Give the preparation type.
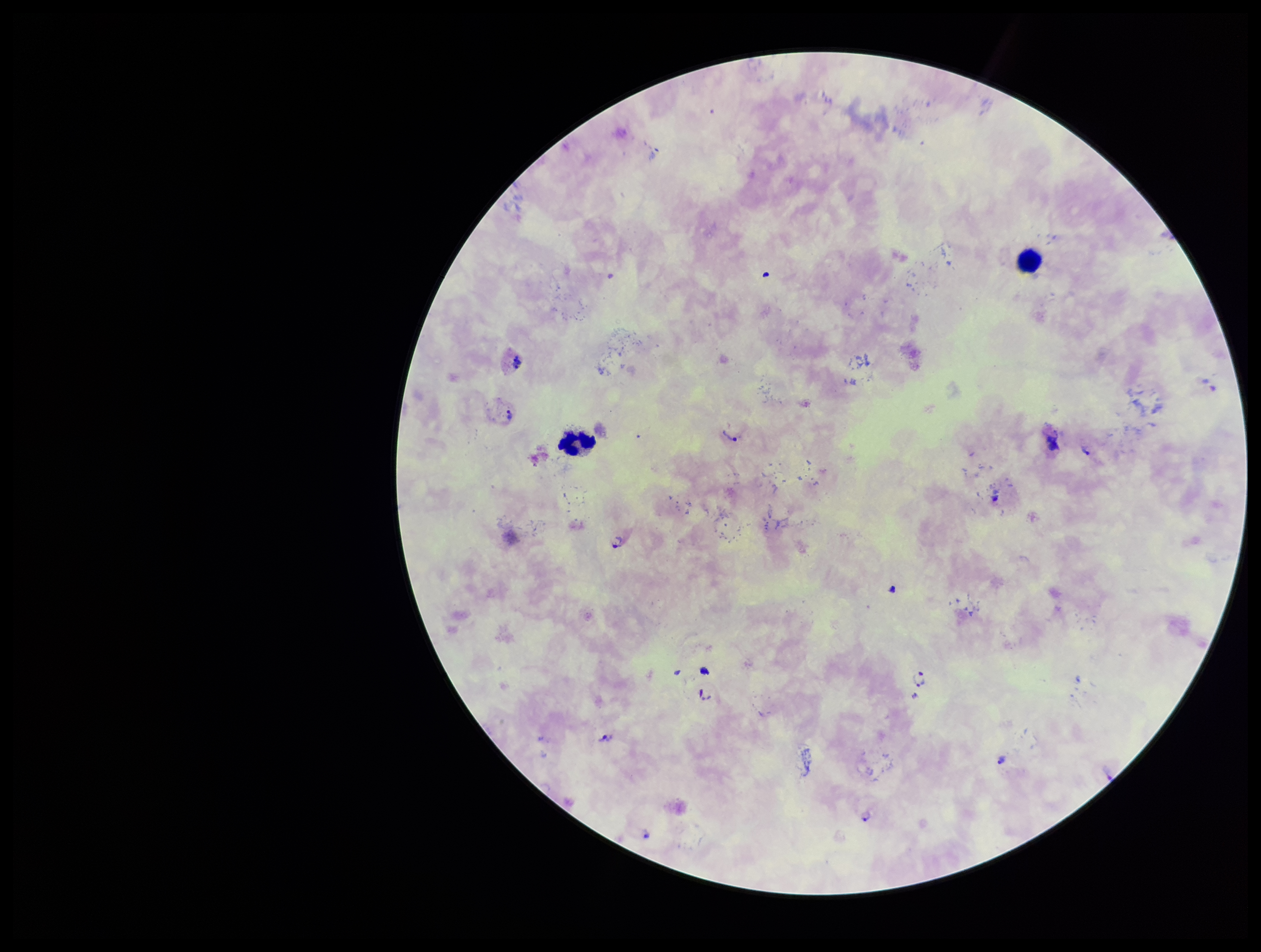

A thick smear.

Plasmodium parasites = identified
field of view = one from this slide
image size = 1261×952 pixels
patient malaria status = infected
leukocyte count = 2
capture = smartphone photograph through the microscope eyepiece
species reported for this patient = Plasmodium vivax
parasite count = 10
stain = Giemsa